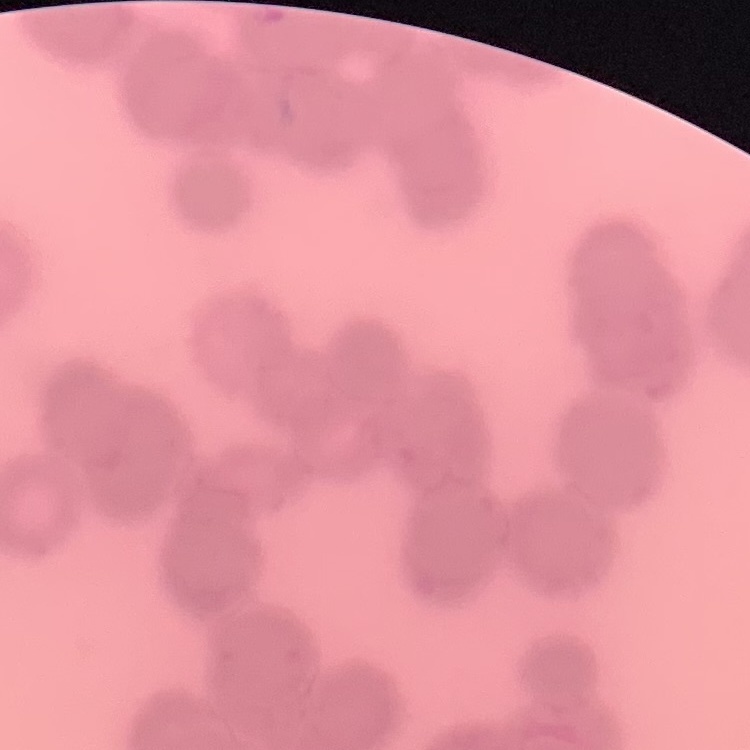

Summary:
  - Red blood cell morphology: rouleaux formation
  - Stain: Field's or Giemsa
  - Image type: one tile cut from a larger photomicrograph
  - Preparation: thin blood film